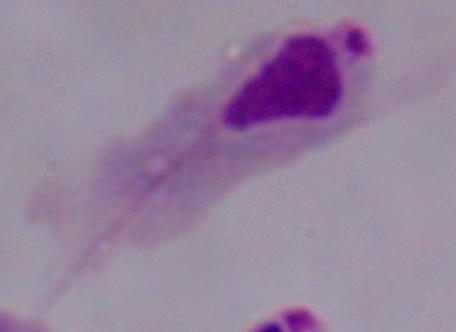
identification = trichomonad
modality = micrograph
magnification = 1000x